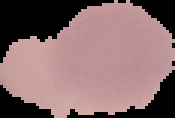
From a thin blood smear. The area outside the segmented cell region is set to black. Result: no malaria parasites detected. Image is 175×118 pixels.